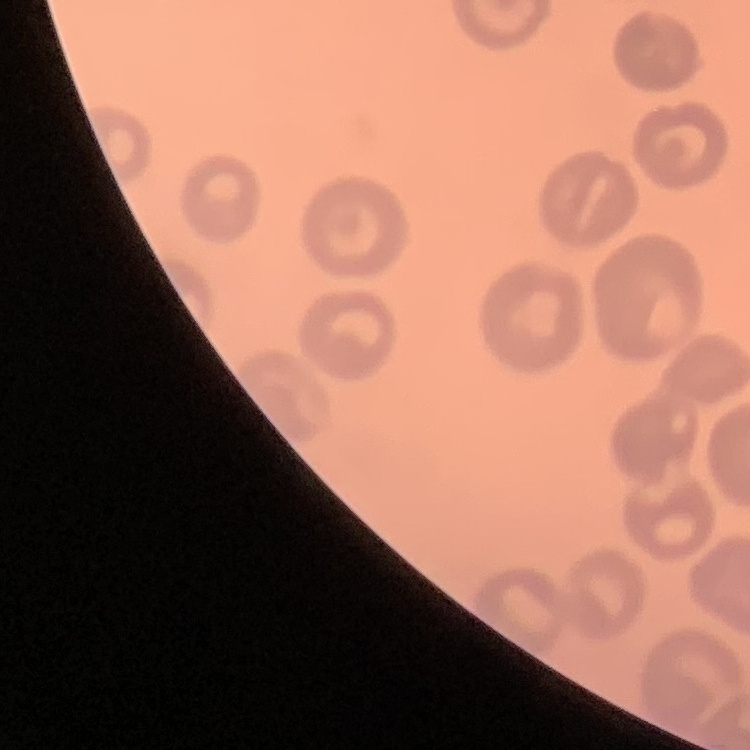
The red blood cells exhibit no rouleaux formation. Thin blood smear. One tile cut from a larger photomicrograph. Field's or Giemsa stain.